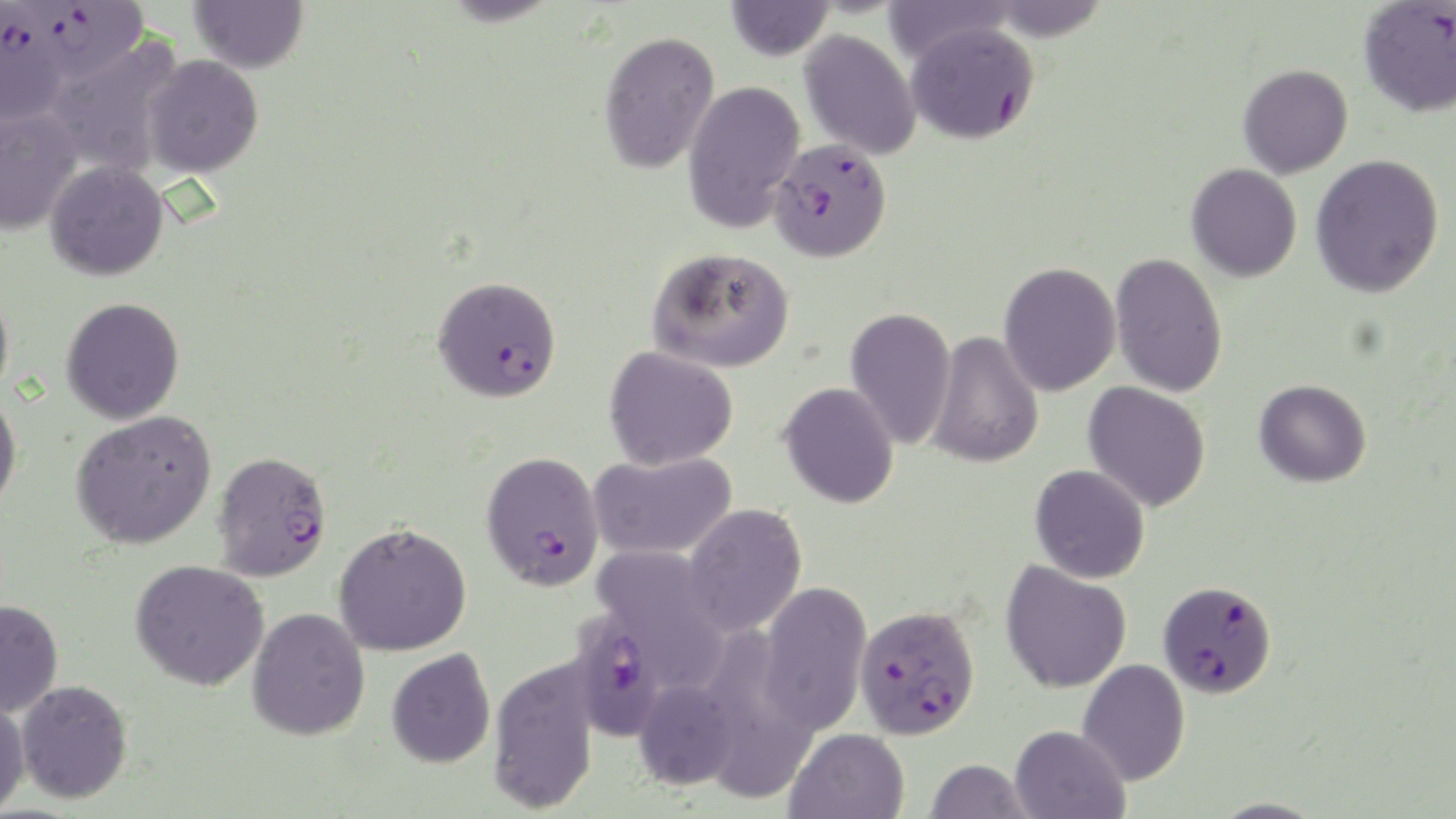 Approximate bounding boxes as [x1, y1, x2, y2] in pixels. Uninfected red blood cell locations: [189, 0, 309, 74], [881, 0, 1014, 65], [985, 0, 1111, 41], [724, 1, 835, 61], [799, 28, 922, 160], [598, 30, 720, 174], [46, 37, 183, 176], [142, 54, 263, 178], [1238, 64, 1353, 178], [683, 80, 805, 234], [0, 107, 82, 236], [1311, 154, 1444, 298], [45, 160, 168, 281], [1186, 164, 1302, 282], [647, 246, 795, 373], [1110, 252, 1228, 398], [998, 262, 1121, 397], [0, 284, 14, 407], [61, 297, 185, 425], [845, 306, 957, 450], [927, 331, 1044, 469], [604, 346, 738, 470], [1254, 379, 1371, 487], [779, 382, 899, 509], [1083, 382, 1211, 512], [0, 392, 22, 514], [70, 410, 216, 549], [587, 451, 738, 560], [1029, 464, 1150, 584], [682, 503, 807, 637], [333, 522, 472, 656], [591, 546, 728, 675], [130, 560, 269, 691], [1000, 560, 1132, 694], [757, 580, 872, 736], [0, 598, 63, 718], [247, 607, 370, 741], [386, 648, 496, 768], [488, 655, 601, 814], [1077, 659, 1190, 786], [634, 678, 740, 789], [15, 679, 134, 804], [0, 695, 31, 817], [1010, 724, 1130, 819], [785, 728, 909, 819], [924, 759, 1034, 818], [1207, 797, 1328, 818]. Plasmodium falciparum-infected red blood cell locations: [1358, 0, 1456, 117], [16, 2, 150, 80], [0, 9, 69, 127], [905, 20, 1040, 145], [764, 139, 889, 264], [432, 275, 562, 404], [211, 450, 332, 582], [480, 450, 605, 592], [1158, 580, 1277, 698], [855, 604, 980, 740], [568, 609, 670, 742]. Slide-level diagnosis: Plasmodium falciparum. Image is 1456×819 pixels. Thin blood smear. May-Grünwald-Giemsa-stained preparation. One field of a larger specimen. Light microscopy. Captured at 1000x magnification.